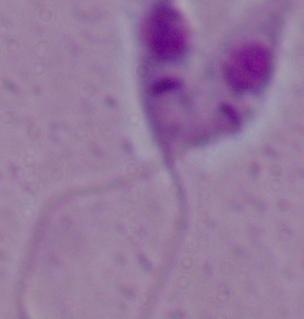
{
  "modality": "micrograph",
  "identification": "Leishmania",
  "magnification": "1000x"
}